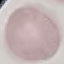

result = negative for malaria parasites
preparation = thin blood smear
stain = Giemsa
capture = smartphone camera at the microscope eyepiece
image type = cell patch, automatically extracted from a larger field of view and resized to 64 × 64 pixels